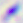
magnification: 400x
identification: Toxoplasma gondii
modality: micrograph